Locate every leukocyte (white blood cell).
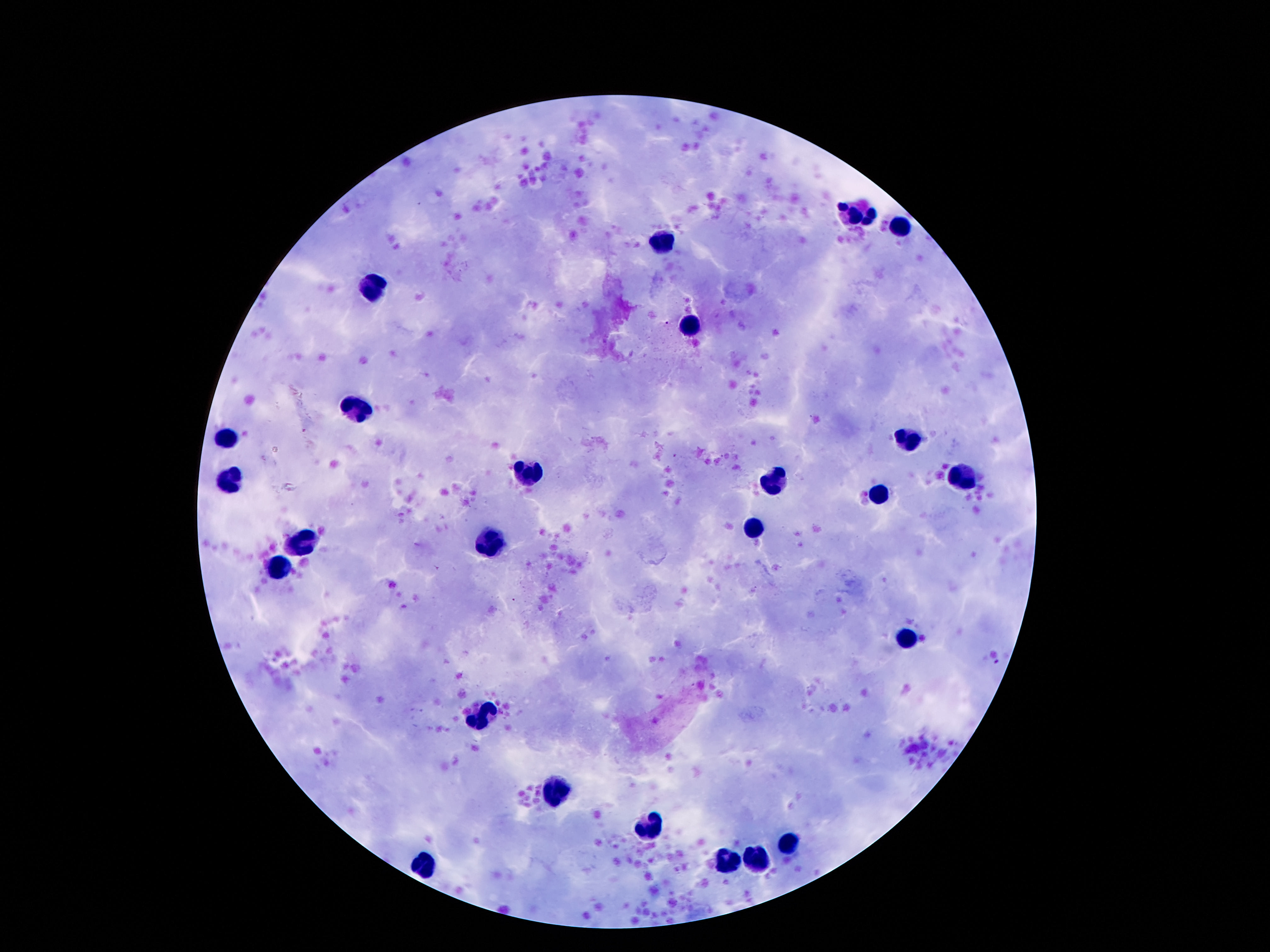
Approximate centers as [x, y] in pixels.
Leukocytes: [864, 215], [901, 228], [665, 244], [377, 287], [687, 326], [355, 411], [227, 435], [906, 438], [519, 473], [963, 478], [773, 480], [227, 482], [875, 496], [751, 531], [304, 540], [488, 544], [276, 569], [908, 641], [481, 717], [552, 794], [647, 825], [791, 843], [758, 861], [722, 863], [424, 868].

One field from this slide. Patient malaria status: negative. Thick blood film. Photographed through the microscope eyepiece with a smartphone camera. Giemsa stain. Image is 1270×952 pixels. 100x magnification.